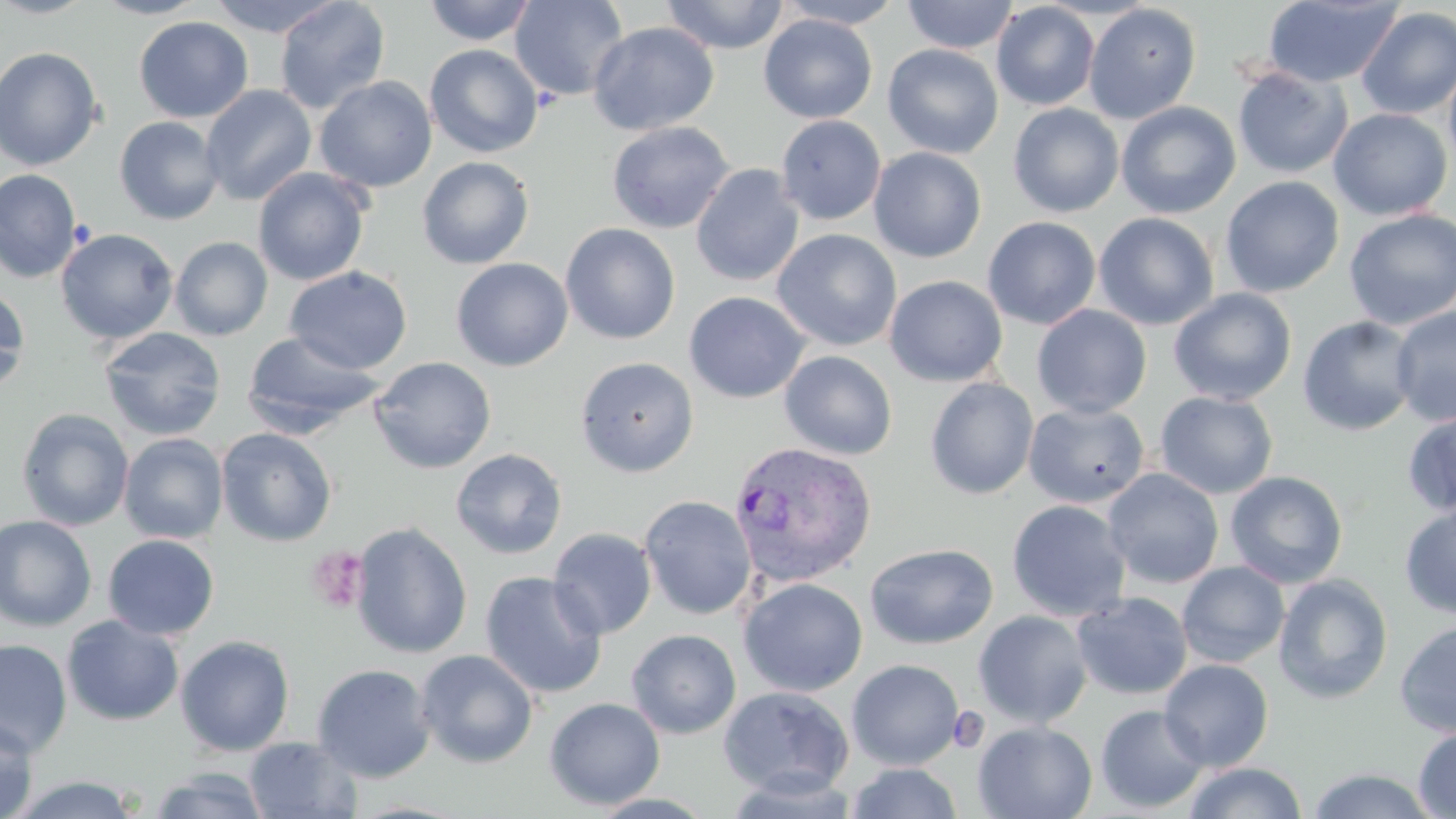 Approximate bounding boxes as (x1,y1)-(x2,y2) corner pairs in pixels. Plasmodium vivax-infected red blood cell locations: (728,441)-(877,587). Uninfected red blood cell locations: (0,0)-(99,19), (91,0)-(210,19), (206,0)-(346,38), (274,0)-(391,114), (422,0)-(538,46), (509,0)-(629,101), (660,0)-(790,54), (774,0)-(906,28), (901,0)-(1018,54), (1263,1)-(1402,88), (992,2)-(1100,110), (1084,3)-(1201,124), (1356,7)-(1456,120), (758,14)-(877,123), (134,16)-(253,123), (587,21)-(720,136), (883,43)-(1003,159), (424,44)-(543,158), (0,46)-(104,171), (1443,56)-(1456,174), (1232,65)-(1352,179), (314,76)-(437,193), (200,84)-(317,206), (1116,101)-(1241,219), (1008,103)-(1124,217), (1327,108)-(1453,221), (776,115)-(886,225), (114,116)-(225,225), (606,121)-(735,234), (868,147)-(987,263), (417,155)-(535,270), (691,164)-(805,287), (252,167)-(371,286), (0,168)-(82,283), (1220,176)-(1344,298), (1343,208)-(1456,330), (1093,212)-(1219,331), (982,216)-(1102,330), (560,223)-(681,344), (55,227)-(179,344), (772,228)-(902,352), (170,236)-(273,341), (451,257)-(573,371), (284,266)-(412,374), (884,275)-(1008,387), (0,284)-(31,396), (1168,288)-(1298,406), (684,291)-(811,404), (1031,304)-(1152,418), (1390,305)-(1456,427), (1298,315)-(1419,436), (98,327)-(227,441), (242,331)-(387,435), (779,350)-(898,460), (368,356)-(497,474), (575,356)-(699,477), (924,378)-(1039,499), (1154,391)-(1278,499), (1024,401)-(1150,508), (17,408)-(135,531), (1401,408)-(1456,517), (215,427)-(337,547), (118,433)-(228,544), (450,448)-(568,559), (1102,468)-(1224,589), (1225,470)-(1349,589), (639,494)-(757,620), (1007,499)-(1132,621), (1399,502)-(1456,620), (0,515)-(97,631), (350,522)-(473,659), (548,527)-(657,640), (102,534)-(219,640), (865,542)-(998,649), (1177,561)-(1290,668), (480,570)-(607,699), (1273,573)-(1394,705), (739,577)-(867,697), (1072,591)-(1193,700), (973,610)-(1093,728), (62,615)-(184,726), (1395,619)-(1456,738), (63,624)-(294,743), (626,629)-(741,739), (175,635)-(295,757), (0,639)-(72,758), (414,649)-(539,768), (847,659)-(964,770), (1159,659)-(1274,771), (311,663)-(436,783), (719,686)-(854,798), (544,697)-(665,810), (1095,704)-(1210,814), (0,716)-(39,819), (973,721)-(1097,819), (1414,726)-(1456,818), (244,736)-(361,818), (1183,761)-(1308,819), (846,762)-(963,819), (147,766)-(272,819), (1305,767)-(1442,819), (9,775)-(142,818). Platelet locations: (305,545)-(370,614). Slide-level diagnosis: Plasmodium vivax. Thin blood smear. One field of a larger specimen. Captured at 1000x magnification. Image is 1456×819 pixels. May-Grünwald-Giemsa stain. Light microscopy.